Name the cell type shown.
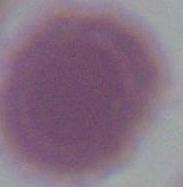
An erythrocyte.

Summary:
  - Modality: photomicrograph
  - Magnification: 1000x